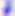

identification = Toxoplasma gondii
magnification = 400x
modality = photomicrograph